Assess this cell for malaria.
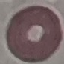
It is uninfected.

stain: Giemsa
preparation: thin blood film
capture: smartphone through the microscope eyepiece
image_type: cell patch, automatically extracted from a larger field of view and resized to 64 × 64 pixels